Mark where platelets are.
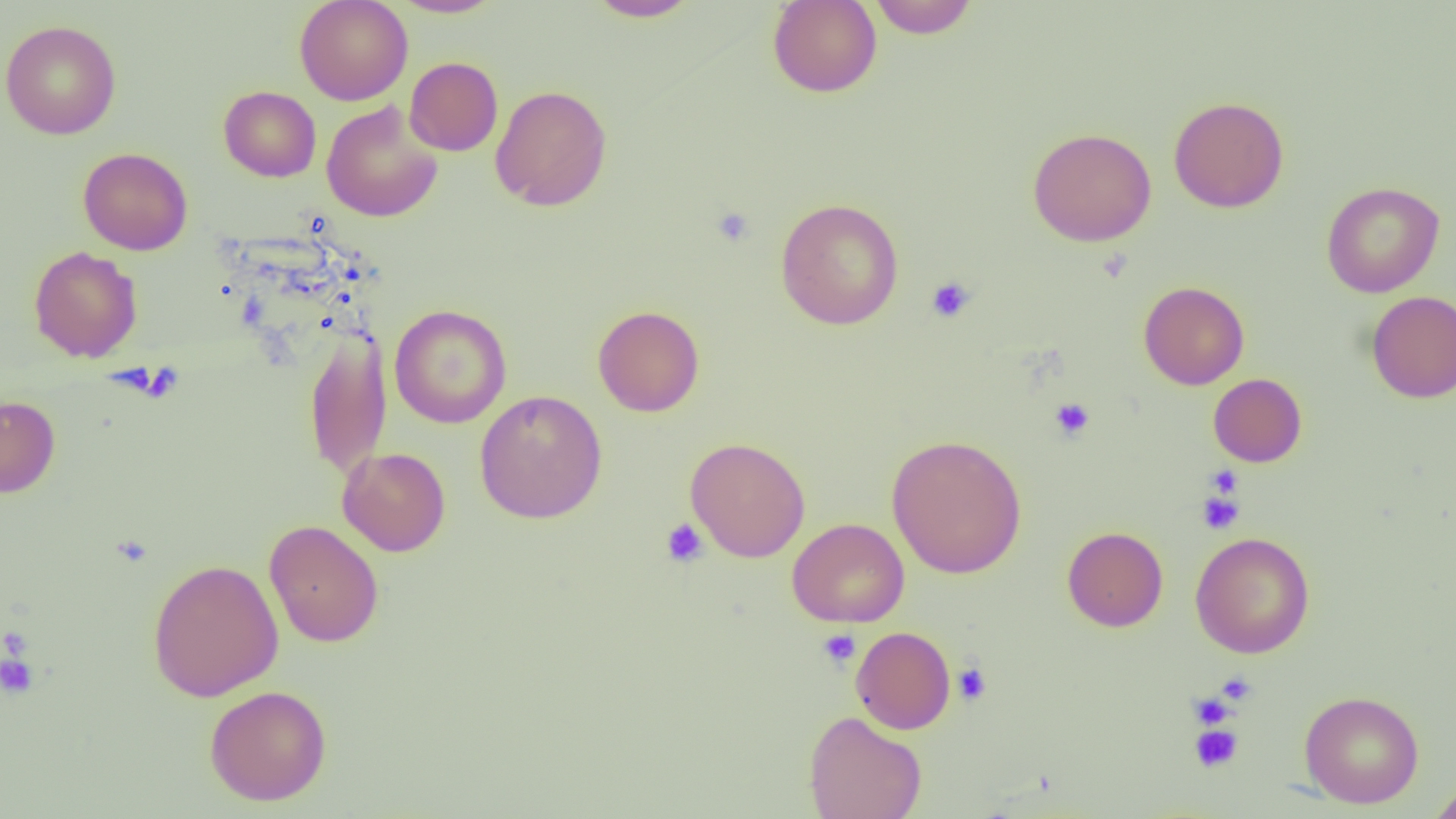
Approximate bounding boxes as [x1, y1, x2, y2] in pixels.
Platelets: [711, 206, 755, 246], [925, 276, 977, 323], [1049, 397, 1095, 441], [1206, 466, 1241, 500], [1197, 490, 1245, 534], [660, 518, 709, 568], [818, 629, 861, 668], [0, 652, 40, 700], [952, 662, 992, 706], [1215, 671, 1258, 705], [1203, 679, 1252, 715], [1188, 692, 1236, 729], [1189, 723, 1243, 773].

Summary:
  - Uninfected red blood cell locations: [294, 0, 413, 105], [389, 0, 504, 18], [584, 0, 702, 22], [767, 0, 882, 98], [866, 1, 979, 38], [1, 20, 121, 140], [405, 57, 503, 156], [490, 84, 613, 212], [218, 86, 321, 182], [1168, 96, 1289, 212], [321, 101, 444, 222], [1027, 127, 1157, 247], [78, 147, 193, 255], [1321, 181, 1445, 298], [775, 198, 904, 329], [28, 246, 142, 362], [1138, 281, 1249, 390], [1366, 290, 1456, 403], [389, 304, 512, 428], [592, 305, 705, 417], [303, 331, 392, 481], [1208, 374, 1307, 467], [474, 389, 608, 524], [0, 394, 60, 498], [886, 434, 1027, 579], [685, 437, 810, 562], [338, 447, 450, 556], [788, 518, 909, 628], [264, 521, 383, 647], [1062, 526, 1168, 632], [1190, 532, 1315, 658], [146, 558, 284, 702], [851, 626, 956, 734], [204, 685, 332, 806], [1299, 690, 1424, 808], [803, 710, 927, 819], [1427, 779, 1456, 819]
  - Slide-level diagnosis: no evidence of blood parasites
  - Image size: 1456×819 pixels
  - Magnification: 1000x
  - Modality: light microscopy
  - Field of view: single
  - Preparation: thin blood smear